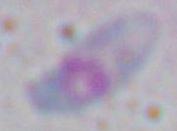
Toxoplasma gondii is seen. Captured at 1000x magnification. Photomicrograph.